Assess the morphology of the red blood cells.
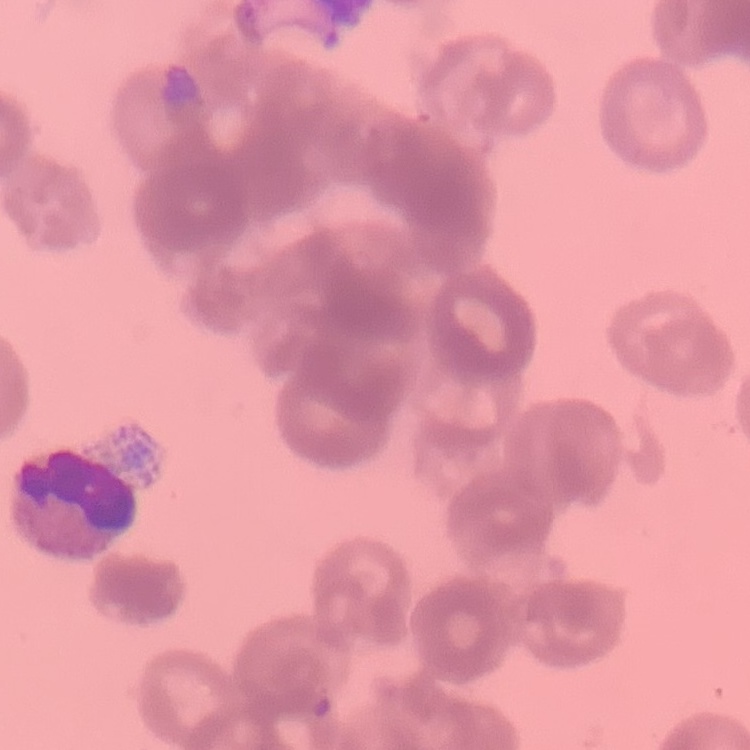
They show rouleaux formation.

Summary:
  - Preparation: thin blood smear
  - Stain: Field's or Giemsa
  - Image type: one tile cut from a larger photomicrograph